Classify this cell by malaria status.
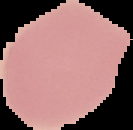
It is uninfected.

Segmented cell region on a black background. From a thin blood film. Image is 133×130 pixels.